Report the malaria status of this cell.
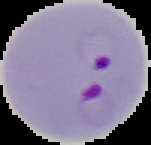
It is parasitized.

image type = segmented cell region with the area outside set to black
preparation = thin blood smear
image size = 151×145 pixels